State the preparation type.
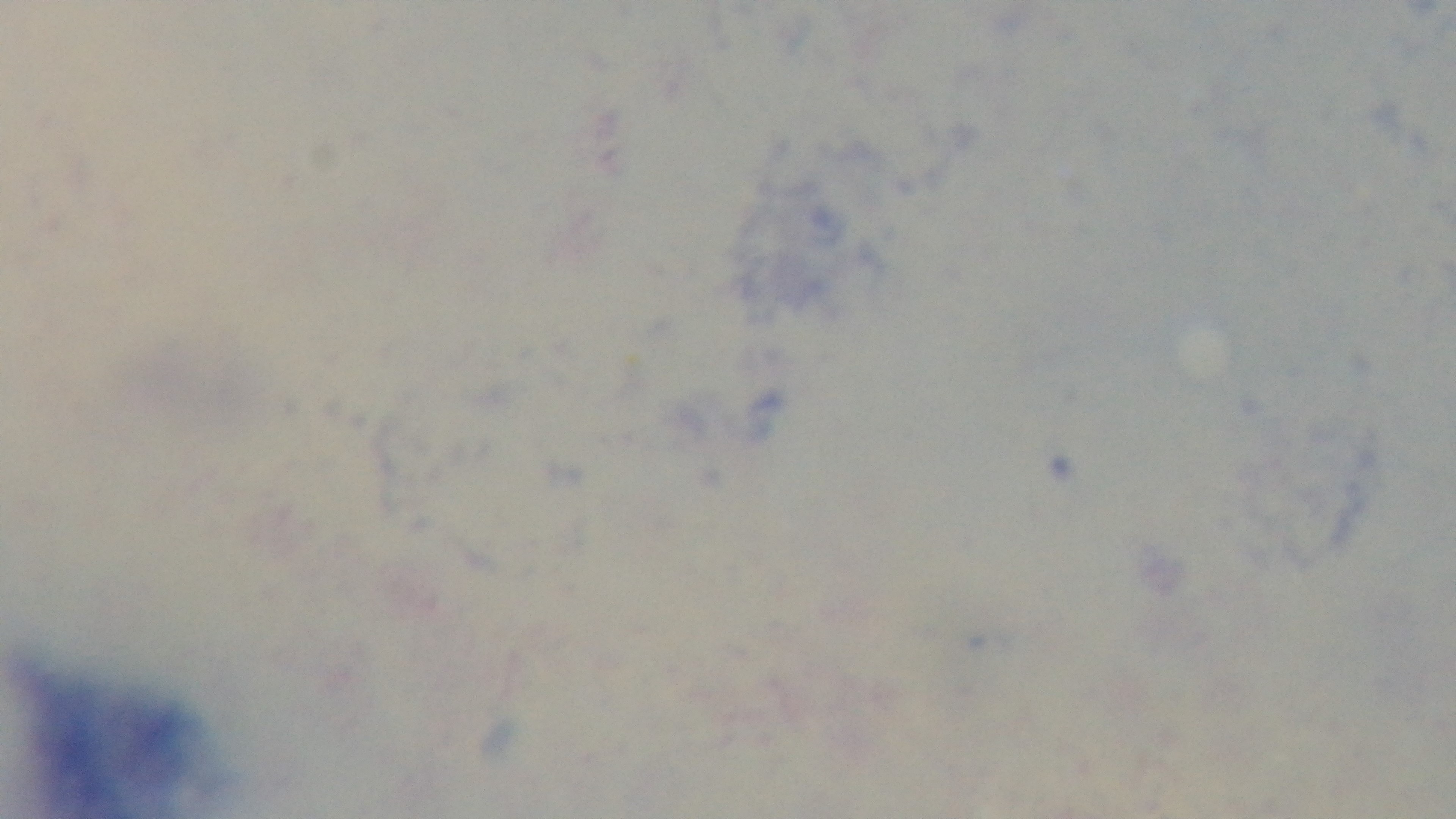

It is a thick blood film.

One field from the slide. Malaria status: negative. Mounted 4K digital camera. Giemsa stain. Light microscopy. Oil-immersion objective, 100x.